Report the malaria status of this cell.
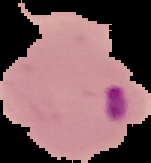
Parasitized.

Summary:
  - Image size: 151×163 pixels
  - Preparation: thin blood film
  - Image type: segmented cell region on a black background